Name the parasite shown.
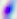
Toxoplasma gondii.

magnification: 400x
modality: micrograph